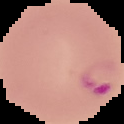

Summary:
  - Preparation: thin blood smear
  - Image type: segmented cell region on a black background
  - Image size: 124×124 pixels
  - Malaria status: parasitized